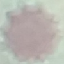

malaria status = uninfected
preparation = thin smear
stain = Giemsa
image type = automatically extracted cell patch, resized to 64 × 64 pixels
capture = smartphone camera at the microscope eyepiece